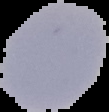
Summary:
  - Malaria status: uninfected
  - Image size: 109×112 pixels
  - Preparation: thin blood film
  - Image type: segmented cell region on a black background